Name the blood parasite species.
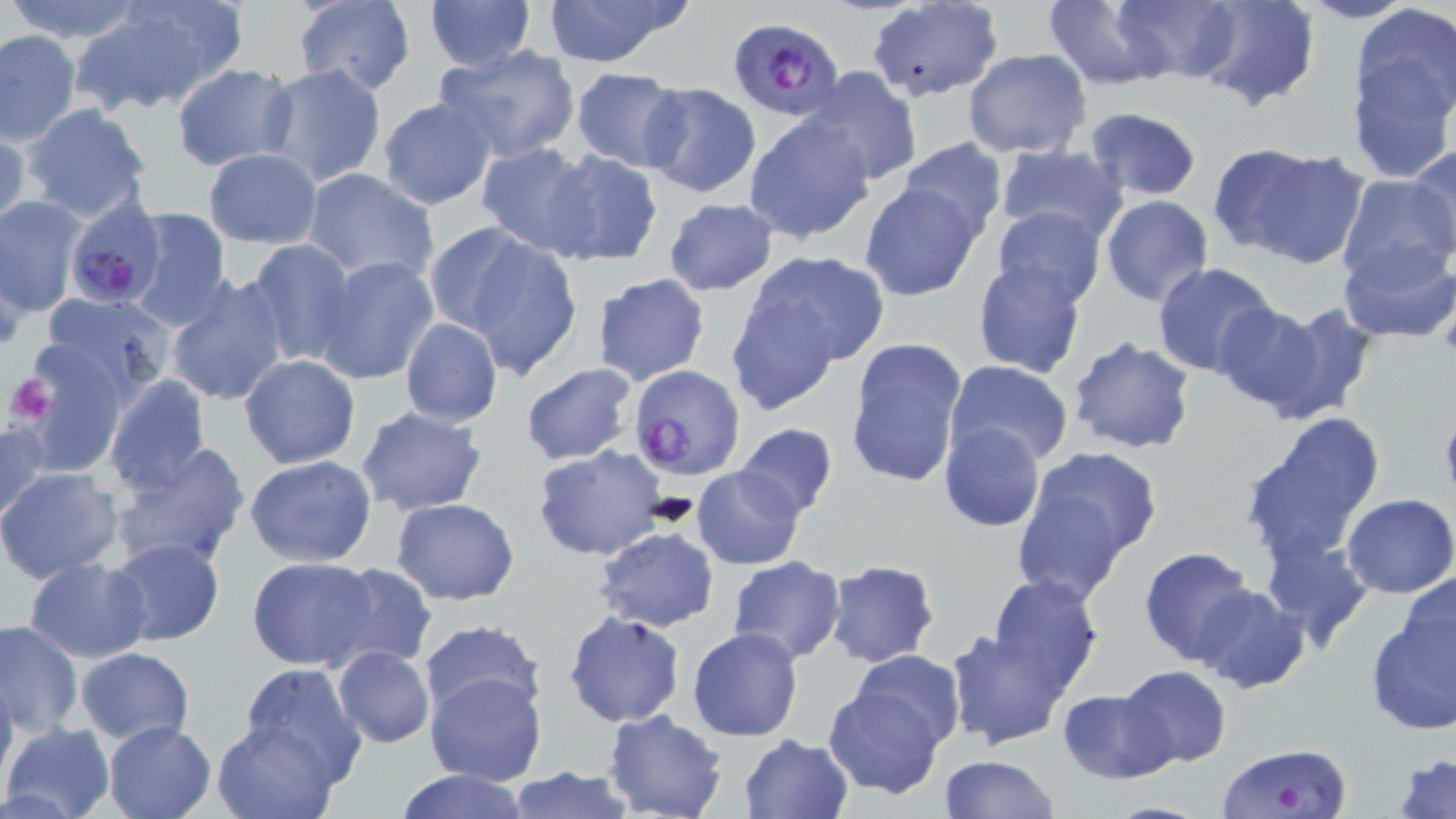

Plasmodium falciparum.

stain = May-Grünwald-Giemsa
field of view = one of a larger specimen
uninfected red blood cell locations = approximate bounding boxes as (x1,y1)-(x2,y2) corner pairs in pixels: (3,0)-(151,45), (75,0)-(244,115), (293,0)-(417,95), (423,0)-(536,73), (536,0)-(695,68), (1042,0)-(1171,89), (1111,0)-(1242,84), (1193,0)-(1320,111), (1296,0)-(1419,23), (1349,0)-(1456,141), (863,1)-(1006,101), (0,29)-(81,146), (432,43)-(581,165), (962,48)-(1093,159), (170,64)-(298,170), (259,64)-(388,189), (568,67)-(687,171), (806,67)-(922,187), (639,83)-(762,198), (377,97)-(497,209), (21,104)-(154,225), (1083,107)-(1203,200), (742,113)-(876,244), (0,122)-(28,235), (896,138)-(1010,238), (1208,141)-(1362,266), (994,142)-(1129,244), (475,143)-(599,257), (1407,144)-(1456,256), (202,148)-(324,248), (542,149)-(664,269), (301,168)-(440,287), (1334,175)-(1456,283), (859,183)-(984,303), (1101,195)-(1214,307), (0,196)-(87,314), (664,199)-(778,295), (990,205)-(1108,310), (129,207)-(232,328), (439,228)-(582,375), (1337,238)-(1454,342), (244,239)-(357,366), (0,241)-(30,348), (741,249)-(889,374), (314,256)-(439,385), (972,258)-(1087,377), (1152,260)-(1281,376), (475,264)-(605,437), (162,272)-(290,407), (590,273)-(710,388), (724,287)-(851,416), (36,290)-(179,403), (1209,302)-(1346,419), (399,317)-(503,427), (1067,337)-(1197,456), (845,338)-(969,490), (22,347)-(130,475), (240,354)-(360,468), (945,359)-(1074,467), (521,363)-(638,464), (101,374)-(212,495), (356,406)-(488,516), (1240,412)-(1385,565), (0,417)-(51,528), (939,422)-(1046,531), (733,423)-(838,522), (110,442)-(252,570), (532,446)-(668,561), (1011,448)-(1163,599), (245,455)-(378,567), (692,465)-(806,570), (1,467)-(123,582), (1343,494)-(1456,597), (390,497)-(520,606), (592,526)-(719,632), (1262,532)-(1376,652), (107,536)-(225,647), (1138,545)-(1257,668), (727,555)-(846,665), (24,557)-(152,663), (244,557)-(381,670), (824,560)-(941,668), (320,561)-(434,671), (1399,573)-(1456,678), (984,575)-(1103,694), (1192,583)-(1309,693), (1364,601)-(1456,736), (564,610)-(685,727), (0,618)-(83,738), (417,618)-(545,721), (687,627)-(804,742), (946,629)-(1072,748), (76,646)-(194,745), (332,646)-(435,748), (847,649)-(966,752), (236,662)-(368,783), (1119,665)-(1231,768), (0,671)-(17,786), (425,672)-(546,786), (823,683)-(947,798), (1058,688)-(1176,781), (602,710)-(727,819), (212,718)-(341,819), (1,721)-(116,819), (103,721)-(215,818), (738,734)-(855,819), (1394,752)-(1456,819), (938,755)-(1058,819), (504,764)-(634,819), (391,768)-(531,819), (1098,800)-(1218,818)
magnification = 1000x
modality = optical microscopy
Plasmodium falciparum-infected red blood cell locations = approximate bounding boxes as (x1,y1)-(x2,y2) corner pairs in pixels: (730,17)-(844,122), (64,200)-(167,309), (629,367)-(744,479), (1213,742)-(1356,819)
image size = 1456×819 pixels
platelet locations = approximate bounding boxes as (x1,y1)-(x2,y2) corner pairs in pixels: (4,372)-(57,424)
preparation = thin blood smear